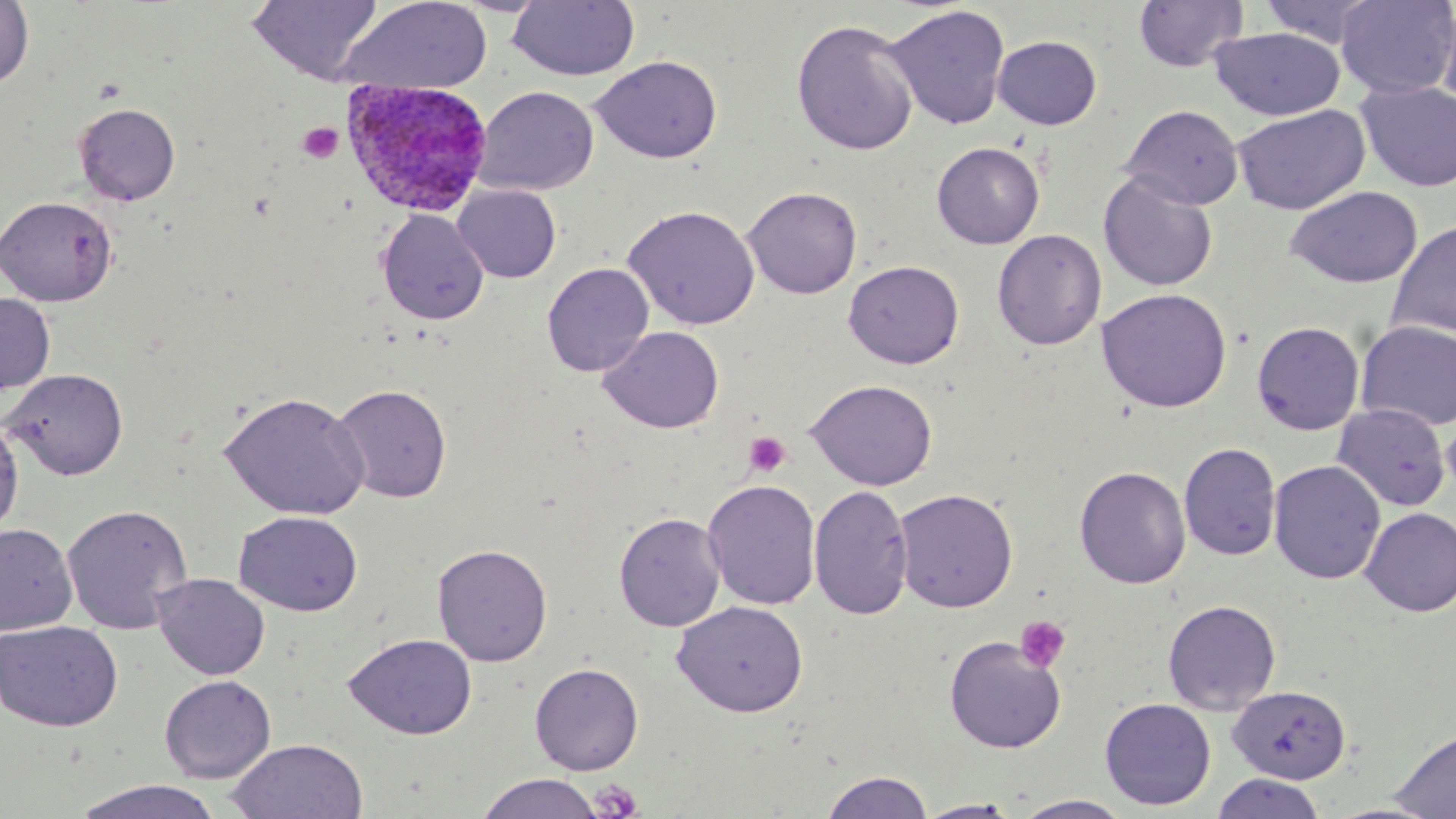
Summary:
  - Coordinate format: approximate bounding boxes as [x1, y1, x2, y2] in pixels
  - Platelet locations: [297, 122, 343, 164], [744, 432, 791, 477], [1015, 615, 1071, 673], [591, 779, 644, 819]
  - Uninfected red blood cell locations: [247, 0, 383, 85], [337, 0, 493, 95], [1132, 0, 1248, 73], [1258, 0, 1384, 48], [1335, 0, 1456, 99], [0, 1, 34, 89], [507, 1, 640, 81], [1436, 1, 1456, 114], [883, 4, 1012, 130], [791, 18, 919, 156], [1209, 27, 1345, 120], [992, 35, 1102, 130], [589, 55, 723, 163], [1357, 81, 1456, 192], [473, 86, 599, 196], [73, 103, 181, 205], [1232, 104, 1370, 215], [1121, 105, 1244, 210], [931, 142, 1045, 249], [1098, 171, 1219, 292], [452, 184, 561, 283], [742, 185, 863, 299], [1286, 186, 1423, 288], [0, 196, 118, 307], [622, 204, 761, 330], [376, 208, 489, 326], [1386, 221, 1455, 343], [992, 229, 1106, 350], [843, 260, 964, 369], [542, 262, 655, 377], [1096, 288, 1232, 413], [0, 292, 56, 394], [1355, 320, 1456, 431], [1251, 321, 1365, 435], [597, 325, 724, 434], [2, 368, 129, 481], [805, 379, 938, 490], [331, 384, 452, 503], [219, 390, 370, 521], [1331, 403, 1451, 511], [1441, 409, 1456, 500], [0, 418, 24, 539], [1179, 442, 1281, 561], [1269, 460, 1386, 584], [1074, 465, 1191, 589], [702, 478, 821, 610], [809, 483, 913, 619], [894, 488, 1018, 612], [61, 503, 193, 634], [1359, 507, 1456, 617], [233, 511, 363, 617], [614, 512, 727, 632], [0, 523, 78, 635], [432, 542, 553, 667], [152, 573, 270, 680], [1163, 599, 1281, 715], [673, 600, 808, 717], [0, 620, 123, 732], [343, 632, 478, 740], [944, 635, 1066, 753], [530, 662, 644, 775], [159, 674, 276, 783], [1227, 685, 1351, 784], [1099, 697, 1216, 811], [1390, 729, 1456, 818], [225, 738, 367, 819], [818, 770, 935, 818], [475, 773, 605, 818], [1210, 773, 1328, 819], [70, 780, 226, 819], [1012, 794, 1134, 818], [915, 798, 1024, 818]
  - Plasmodium ovale-infected red blood cell locations: [341, 80, 491, 217]
  - Slide-level diagnosis: Plasmodium ovale
  - Modality: optical microscopy
  - Magnification: 1000x
  - Image size: 1456×819 pixels
  - Field of view: one of a larger specimen
  - Stain: May-Grünwald-Giemsa
  - Preparation: thin blood film